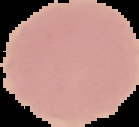

Summary:
  - Image type: cell region segmented out of the field of view; surrounding area masked to black
  - Image size: 139×127 pixels
  - Malaria status: uninfected
  - Preparation: thin blood film